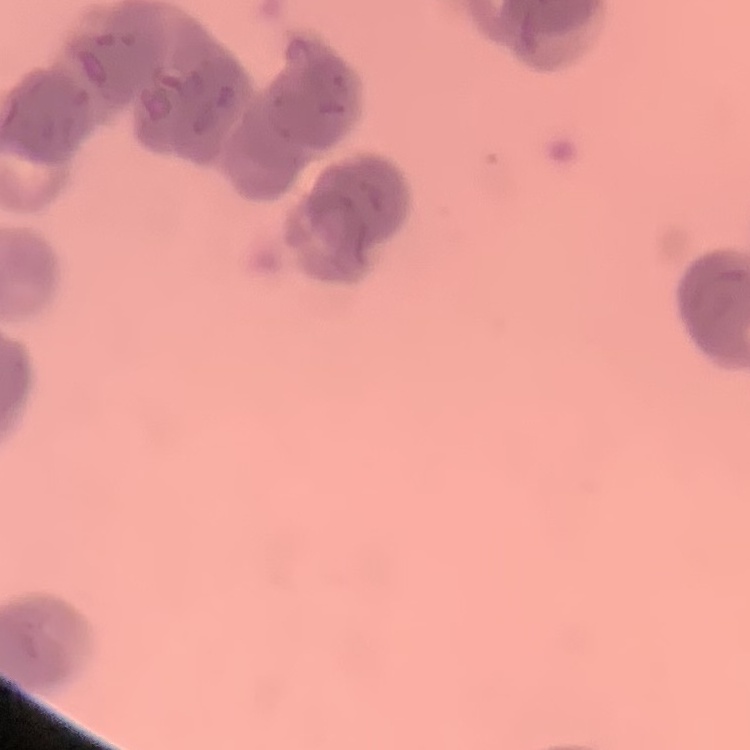
The erythrocytes show rouleaux formation. Stained with either Field's or Giemsa. Thin blood smear. Square crop of a larger photomicrograph.